State which parasite is depicted.
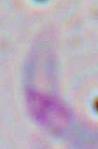
Toxoplasma gondii.

Captured at 1000x magnification. Photomicrograph.